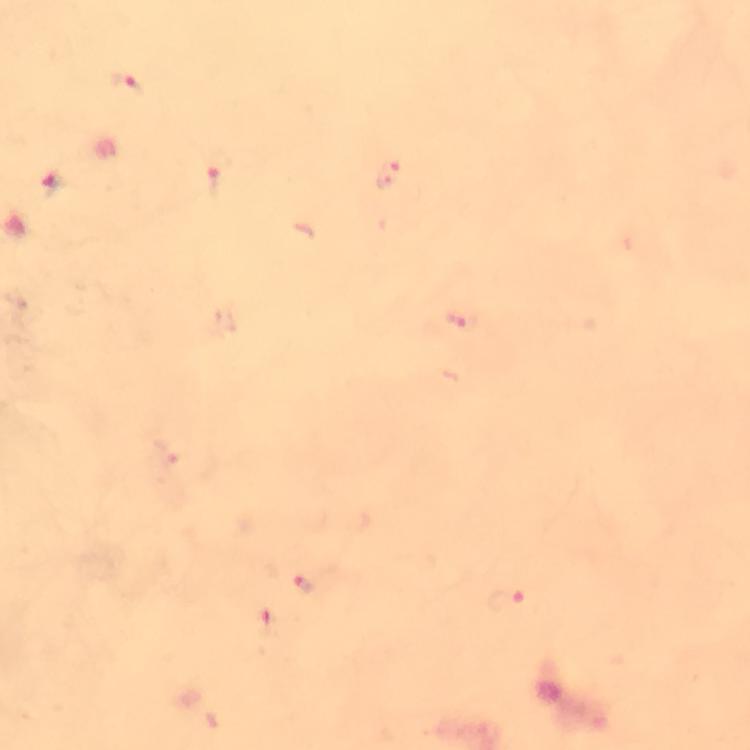
Approximate object centers, in pixels from the top-left corner. Malaria parasite locations: (x=127, y=86), (x=389, y=176), (x=53, y=183), (x=212, y=183), (x=459, y=322), (x=303, y=584), (x=507, y=599). Photographed through the microscope with a smartphone camera. Image is 750×750 pixels. Giemsa stain. From a diagnostic examination for malaria. Immersion oil was used. Thick smear. At 100x magnification. Cropped region of a single field of view.